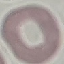
Malaria status: uninfected. Thin blood film. Giemsa-stained preparation. Photographed with a smartphone camera at the microscope eyepiece. Automatically extracted cell patch, resized to 64 × 64 pixels.